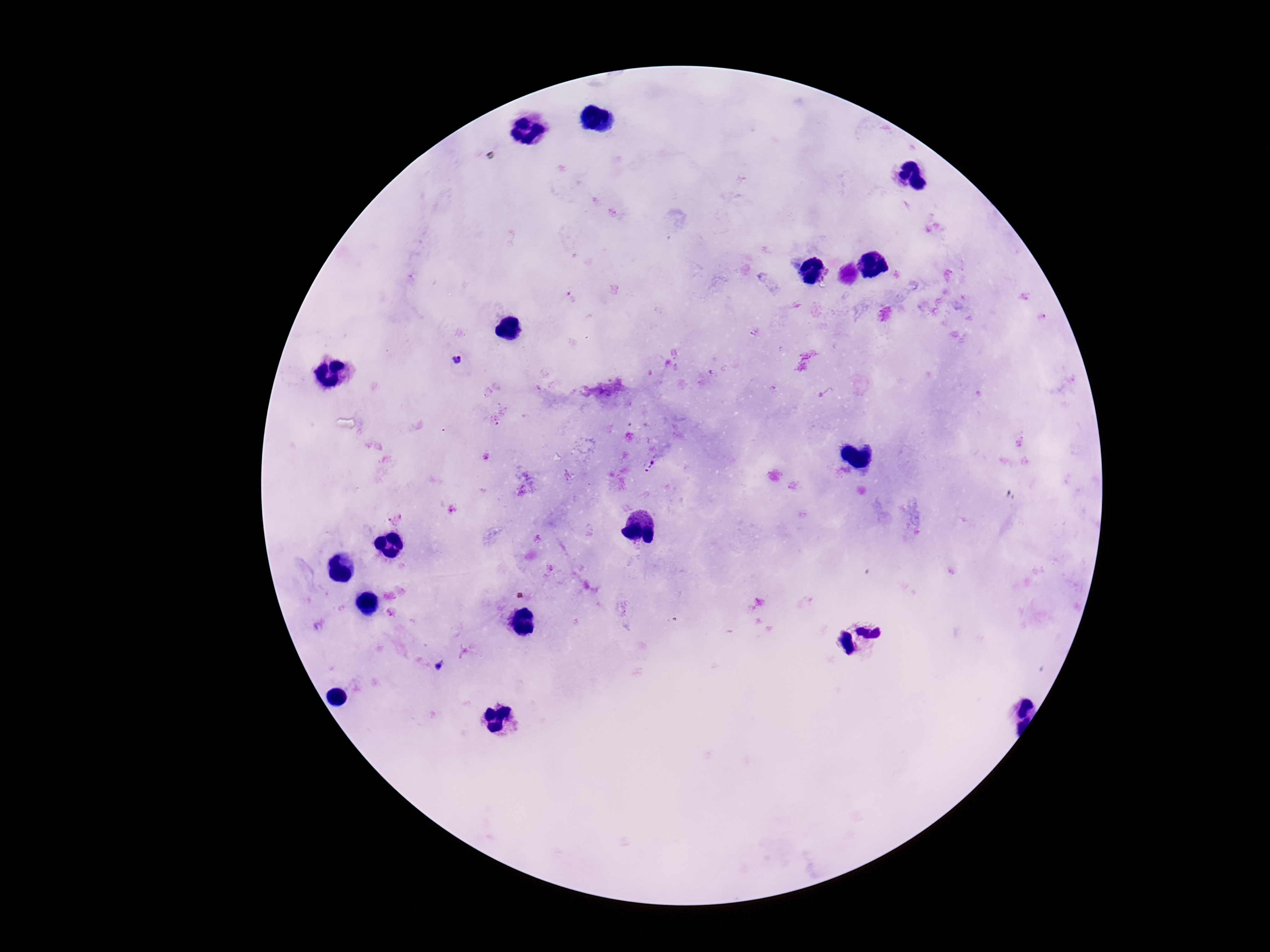

Approximate centers as {x, y} in pixels. Plasmodium parasite locations: {754, 332}, {459, 361}, {652, 465}, {440, 666}. Smartphone photograph taken through the microscope eyepiece. Thick peripheral-blood smear. Image is 1270×952 pixels. Single field of view. 100x magnification. Giemsa-stained preparation. Patient malaria status: positive.